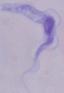 Photomicrograph. A trypanosome is shown. 1000x magnification.